Describe the morphology of the erythrocytes.
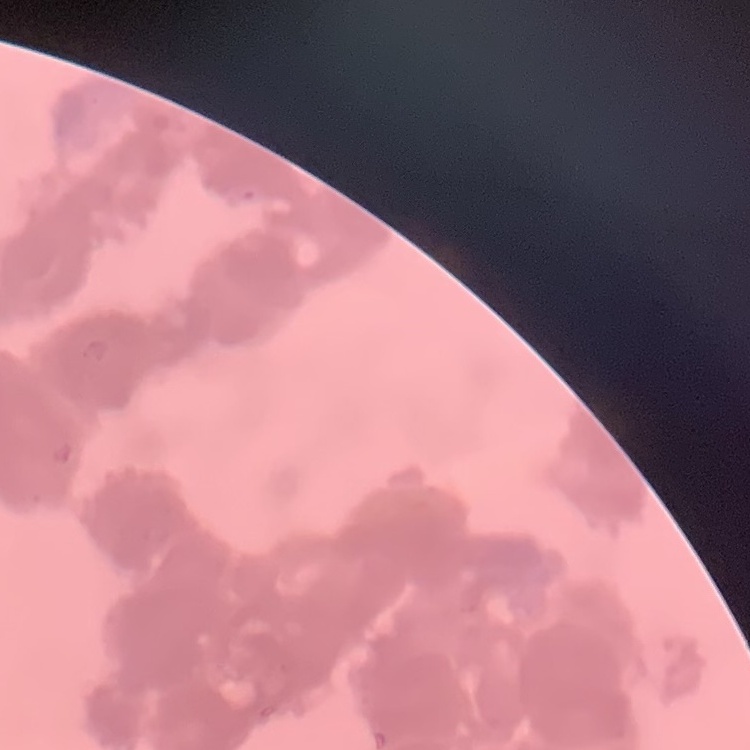
They show rouleaux formation.

stain = Field's or Giemsa
preparation = thin blood film
image type = one tile cut from a larger photomicrograph